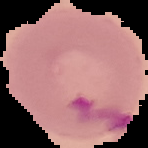
The area outside the segmented cell region is set to black. Malaria status: parasitized. From a thin blood smear. Image is 148×148 pixels.